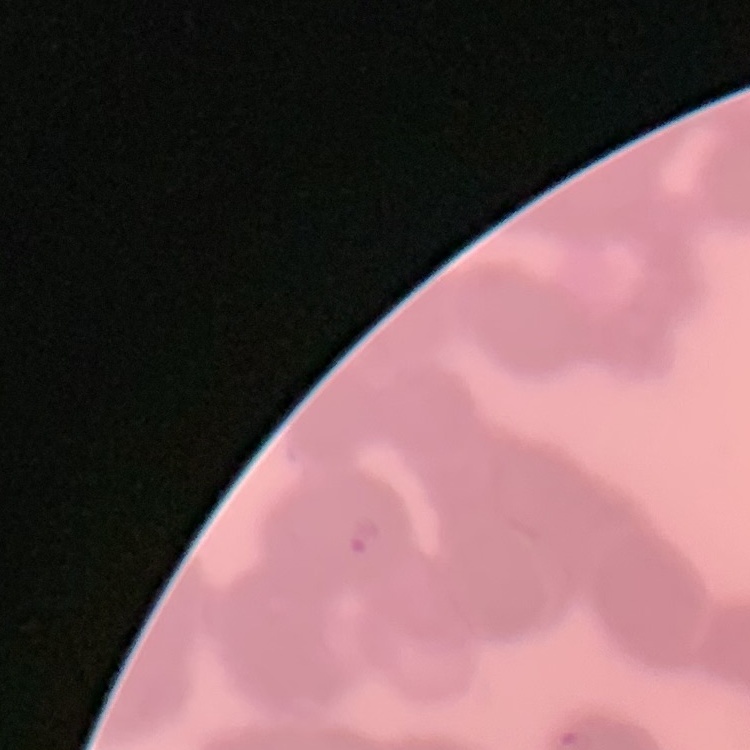

Summary:
  - Red blood cell morphology: rouleaux formation
  - Stain: Field's or Giemsa
  - Preparation: thin blood smear
  - Image type: square crop of a larger photomicrograph